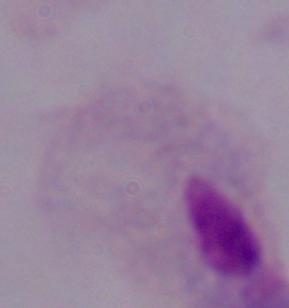 A trichomonad is seen. 1000x magnification. Micrograph.